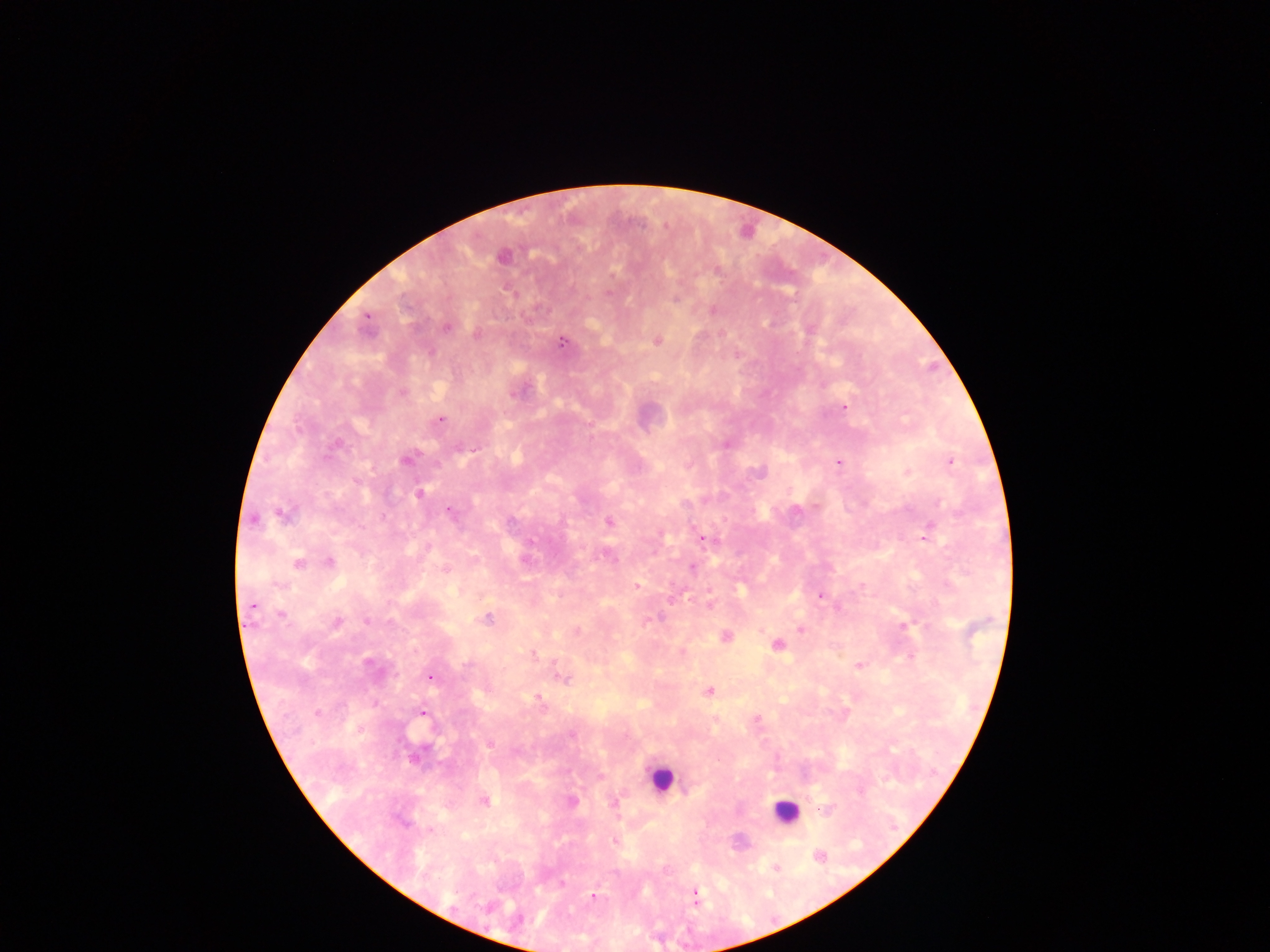
malaria parasite locations = approximate centers as {x, y} in pixels: {502, 257}, {608, 293}, {713, 310}, {366, 317}, {447, 326}, {477, 335}, {656, 340}, {562, 342}, {402, 394}, {513, 394}, {844, 407}, {441, 419}, {589, 437}, {338, 444}, {726, 444}, {474, 449}, {405, 460}, {839, 462}, {950, 462}, {759, 472}, {419, 493}, {449, 510}, {282, 515}, {254, 519}, {609, 522}, {925, 536}, {702, 539}, {531, 541}, {329, 562}, {298, 564}, {692, 568}, {445, 569}, {637, 586}, {820, 596}, {710, 604}, {251, 605}, {281, 614}, {487, 619}, {366, 621}, {336, 622}, {904, 626}, {801, 629}, {577, 631}, {760, 632}, {725, 637}, {777, 645}, {682, 652}, {533, 654}, {910, 656}, {368, 663}, {553, 663}, {466, 665}, {858, 665}, {430, 677}, {564, 679}, {710, 691}, {538, 697}, {541, 702}, {317, 713}, {423, 713}, {758, 719}, {572, 735}, {489, 744}, {600, 777}, {484, 801}, {571, 801}, {615, 803}, {431, 830}, {613, 841}, {818, 856}, {776, 868}, {562, 883}, {694, 895}, {593, 897}
preparation = thick blood film
leukocyte locations = approximate centers as {x, y} in pixels: {661, 778}, {785, 812}
country = Ghana
field of view = single
image size = 1270×952 pixels
capture = mobile-phone photograph through a microscope